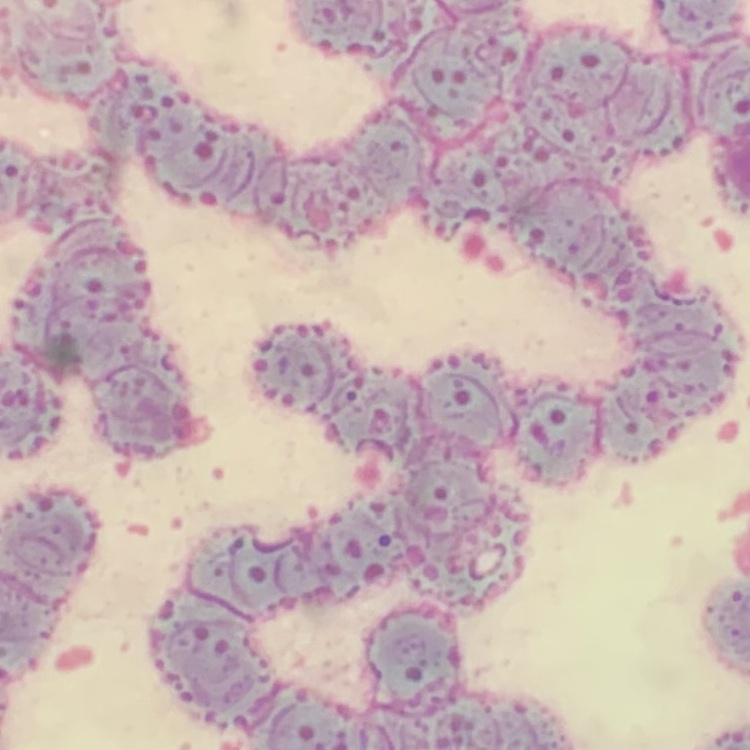
Summary:
  - Erythrocyte morphology: rouleaux formation
  - Image type: one tile cut from a larger photomicrograph
  - Preparation: thin blood film
  - Stain: Field's or Giemsa